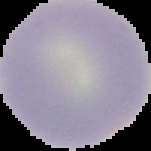
Summary:
  - Image type: cell region segmented out of the field of view; surrounding area masked to black
  - Preparation: thin blood film
  - Image size: 151×151 pixels
  - Result: no Plasmodium parasites detected